Report the malaria status of this cell.
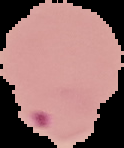

Parasitized.

Summary:
  - Image type: segmented cell region on a black background
  - Image size: 124×148 pixels
  - Preparation: thin blood film